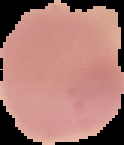
Cell region segmented out of the field of view; the surrounding area is masked to black. Image is 124×145 pixels. Malaria status: uninfected. From a thin blood film.